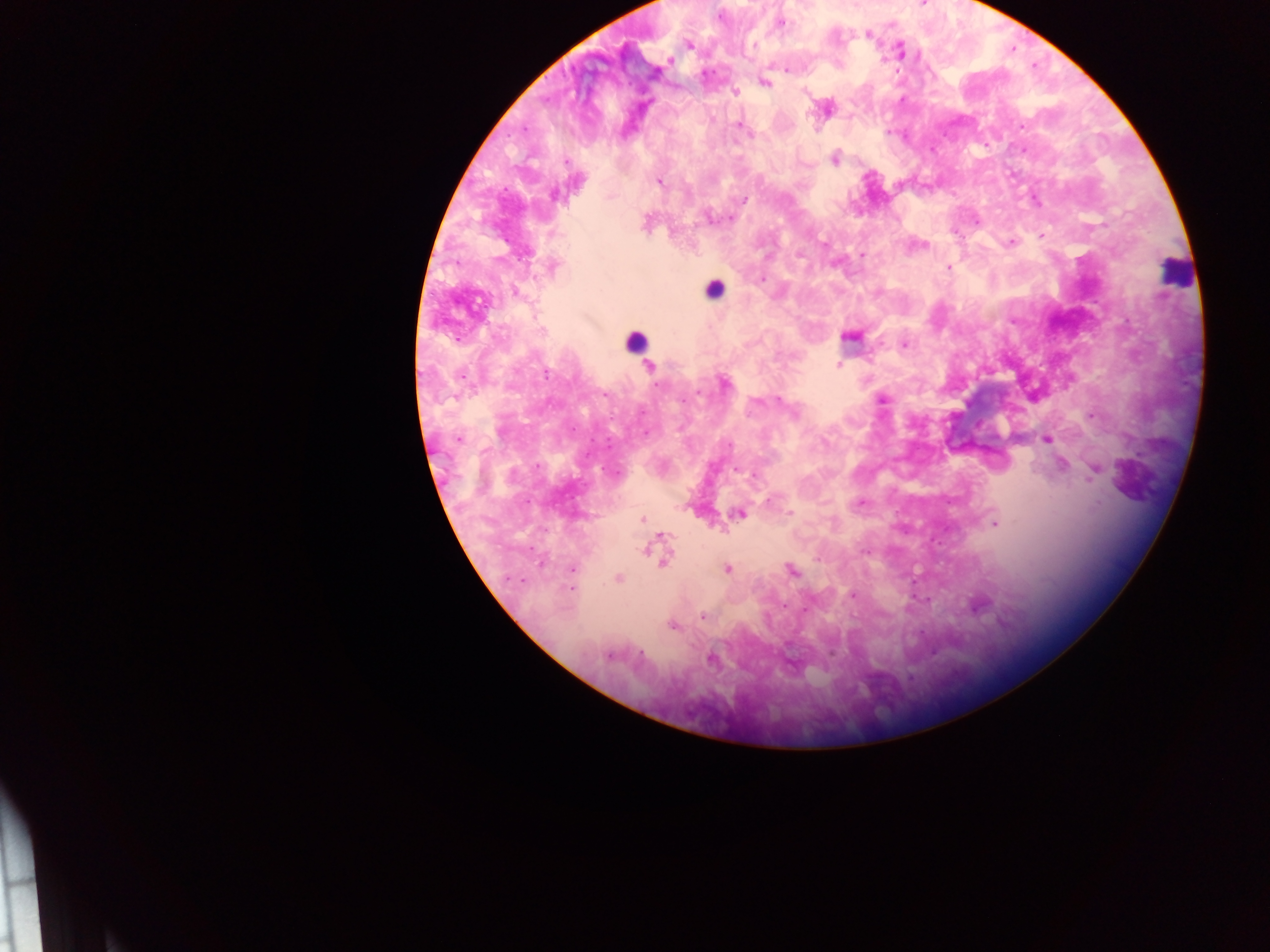
Approximate centers as (x, y) in pixels. Malaria parasite locations: (782, 23), (869, 34), (689, 45), (901, 51), (670, 61), (786, 70), (764, 83), (735, 92), (739, 126), (748, 134), (835, 160), (567, 161), (659, 182), (555, 195), (744, 199), (708, 217), (1042, 235), (1011, 242), (824, 243), (798, 255), (862, 255), (553, 267), (949, 268), (763, 279), (516, 292), (850, 336), (903, 344), (839, 364), (649, 367), (546, 375), (725, 384), (697, 393), (882, 399), (778, 400), (459, 439), (1047, 439), (729, 445), (1063, 466), (735, 469), (1095, 470), (754, 475), (769, 500), (862, 501), (739, 514), (790, 514), (642, 520), (995, 524), (661, 536), (645, 550), (866, 552), (664, 561), (572, 569), (727, 569), (791, 570), (618, 579), (521, 580), (572, 588), (852, 595), (784, 605), (805, 609), (703, 617), (672, 625), (641, 653), (608, 657), (711, 659). Leukocyte locations: (1174, 271), (713, 289), (634, 340). Image is 1270×952 pixels. Sample from Ghana. Thick blood film. Photographed through a microscope with a mobile-phone camera. One field of view.